Identify the preparation type.
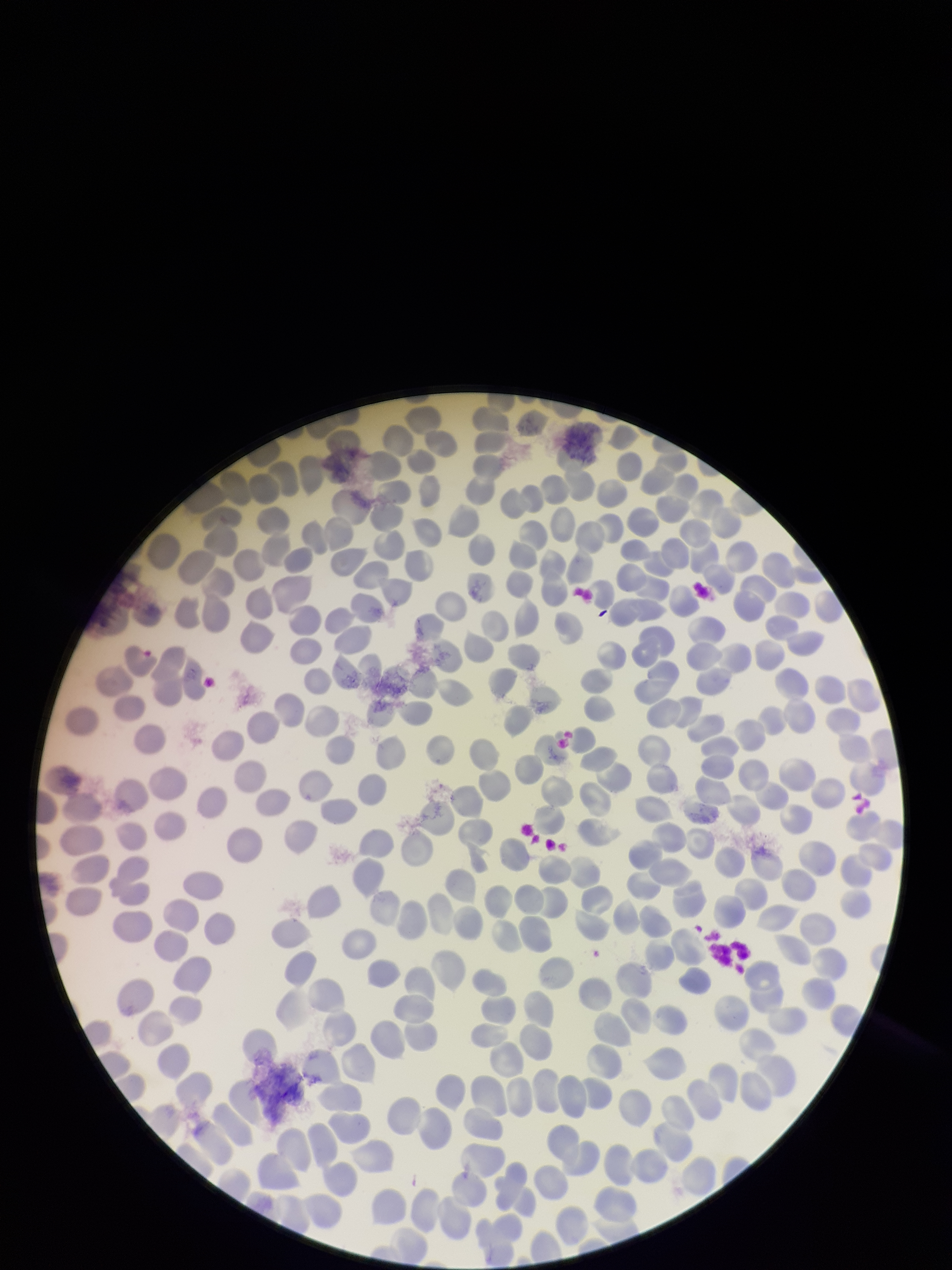

Thin.

image size = 952×1270 pixels
field of view = one from this slide
capture = smartphone photograph through the microscope eyepiece
parasitized red blood cell count = 0
red blood cell count = 325
stain = Giemsa
parasitized red blood cells = none seen
patient malaria status = negative